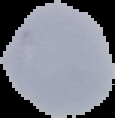

Summary:
  - Image type: segmented cell region on a black background
  - Preparation: thin blood smear
  - Image size: 115×118 pixels
  - Result: no malaria parasites detected